Classify this cell by malaria status.
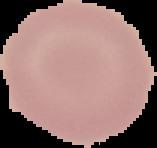
Uninfected.

image size = 157×148 pixels
preparation = thin blood film
image type = segmented cell region with the area outside set to black